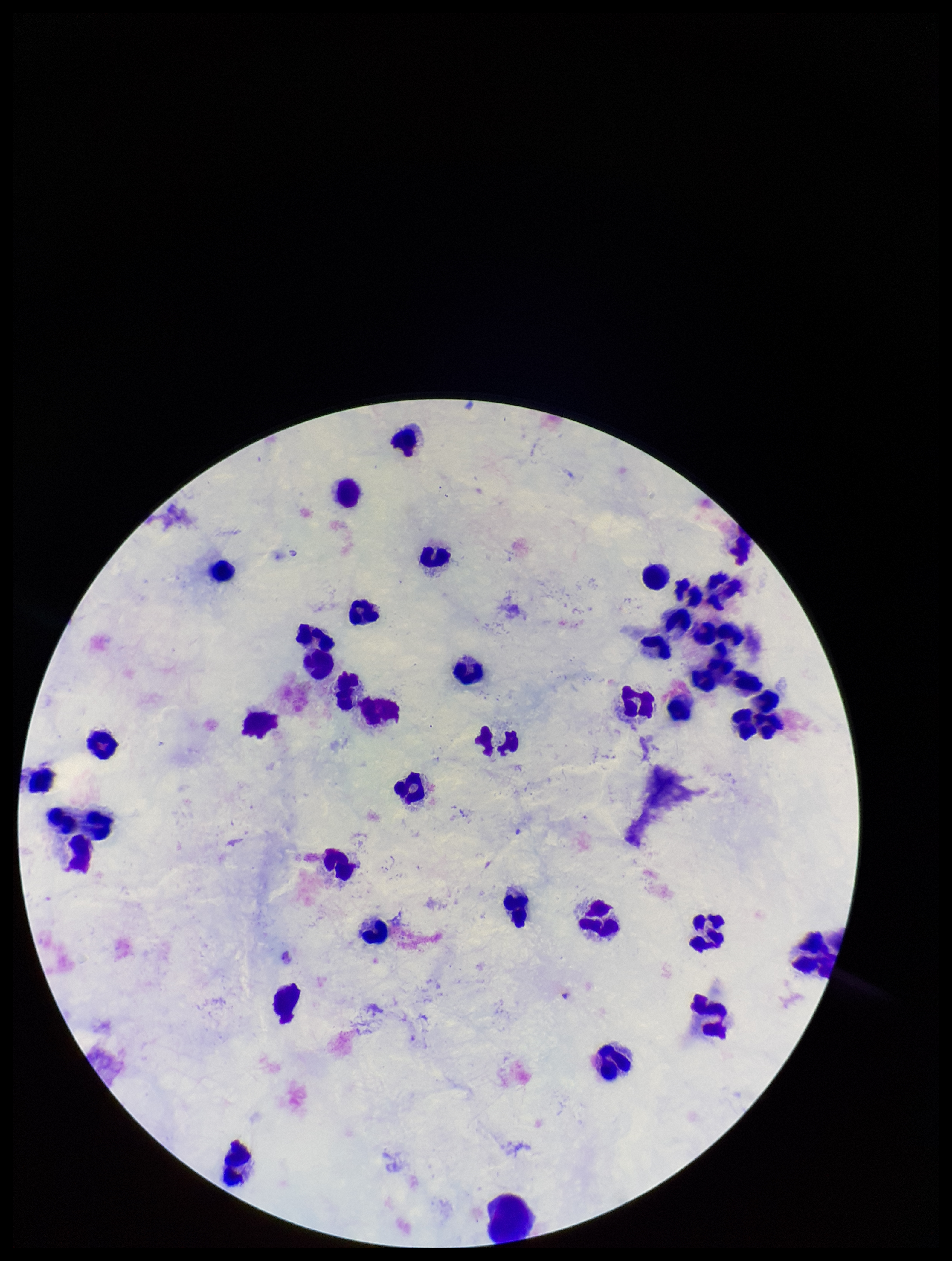
Summary:
  - Plasmodium parasites: none identified
  - Parasite count: 0
  - Patient malaria status: negative
  - Image size: 952×1261 pixels
  - Leukocyte count: 38
  - Field of view: one from this slide
  - Capture: smartphone photograph through the microscope eyepiece
  - Preparation: thick blood smear
  - Stain: Giemsa